Identify the preparation type.
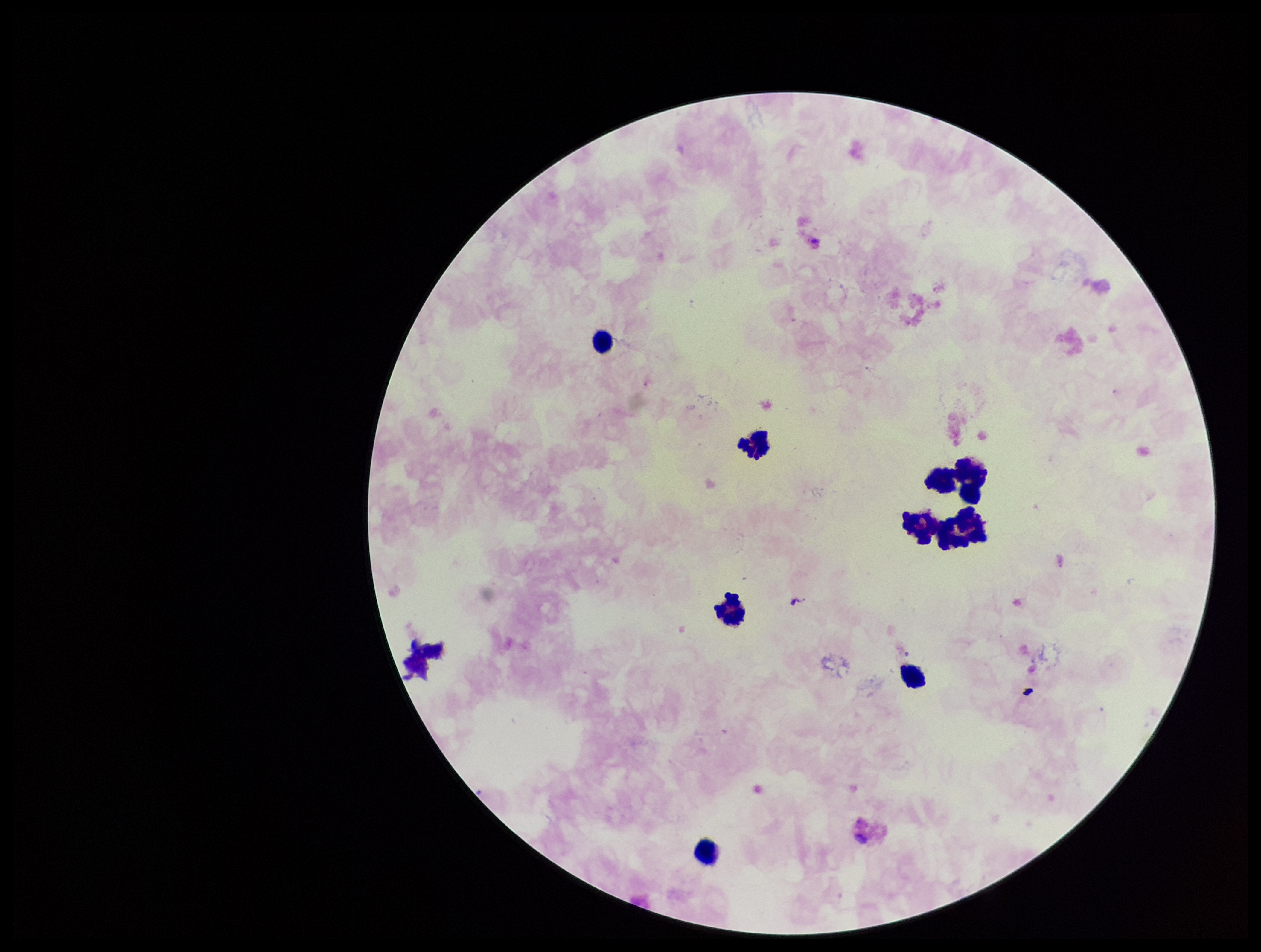

A thick smear.

Plasmodium parasites: none detected. Stained with Giemsa. Parasite count: 0. Patient malaria status: negative. One field from this slide. Leukocyte count: 9. Photographed through the microscope eyepiece with a smartphone camera. Image is 1261×952 pixels.